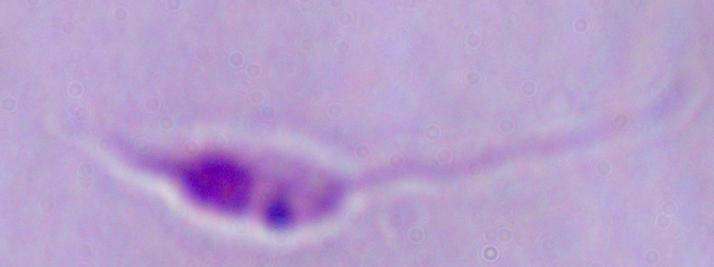
magnification = 1000x
modality = micrograph
identification = Leishmania